Classify this cell by malaria status.
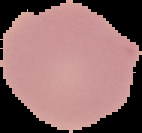

It is uninfected.

image_size: 142×133 pixels
image_type: cell region segmented out of the field of view; surrounding area masked to black
preparation: thin blood smear